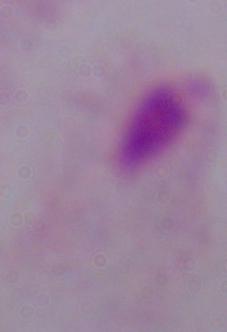 Micrograph. Captured at 1000x magnification. A trichomonad is seen.